Assess this cell for malaria.
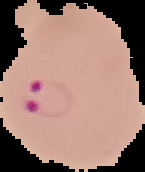

Parasitized.

From a thin blood film. Image is 145×172 pixels. The area outside the segmented cell region is set to black.